Point out each Plasmodium parasite.
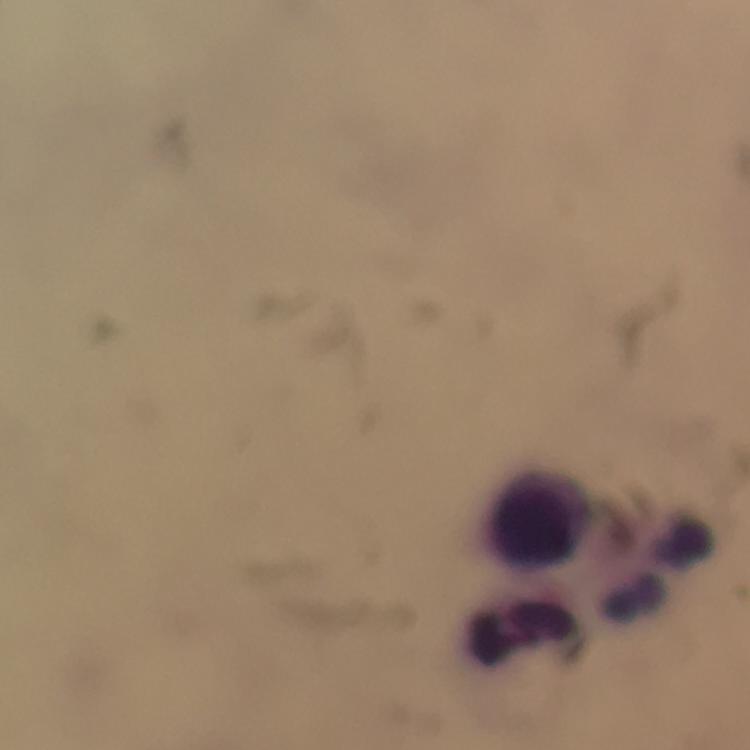
No Plasmodium parasites seen.

Approximate centers as {x, y} in pixels. Leukocyte locations: {540, 515}, {661, 568}, {525, 634}. Image is 750×750 pixels. Cropped region of a single field of view. Thick smear. From a malaria diagnostic workup. Giemsa stain. Immersion oil applied. Smartphone photograph taken through a microscope. 100x magnification.